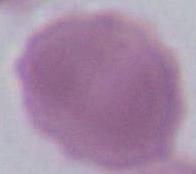 A red blood cell is seen. Photomicrograph. Captured at 1000x magnification.